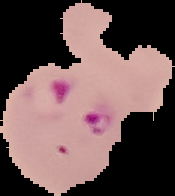

Malaria status: parasitized. From a thin blood smear. Segmented cell region on a black background. Image is 175×196 pixels.